Classify this cell by malaria status.
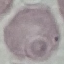

Uninfected.

Cell patch, automatically extracted from a larger field of view and resized to 64 × 64 pixels. Photographed with a smartphone camera at the microscope eyepiece. Thin smear of blood. Giemsa-stained preparation.